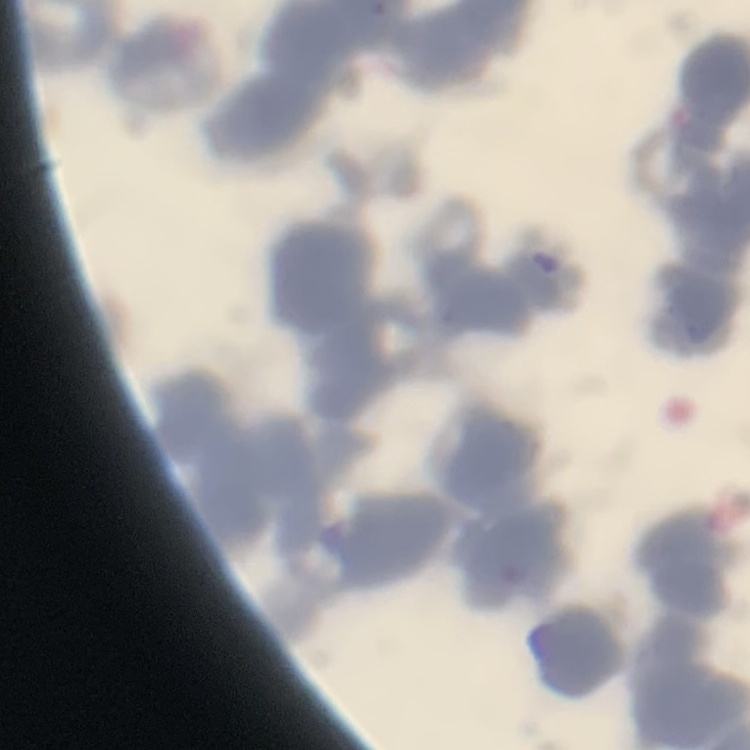

Summary:
  - Red blood cell morphology: rouleaux formation
  - Stain: Field's or Giemsa
  - Preparation: thin blood smear
  - Image type: square crop of a larger photomicrograph